Report the malaria status of this cell.
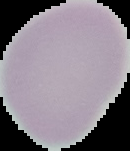
It is uninfected.

Cell region segmented out of the field of view; the surrounding area is masked to black. Image is 130×151 pixels. From a thin blood smear.